Assess this cell for malaria.
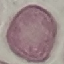
Uninfected.

image_type: cell patch, automatically extracted from a larger field of view and resized to 64 × 64 pixels
stain: Giemsa
preparation: thin blood smear
capture: smartphone through the microscope eyepiece